Assess the morphology of the erythrocytes.
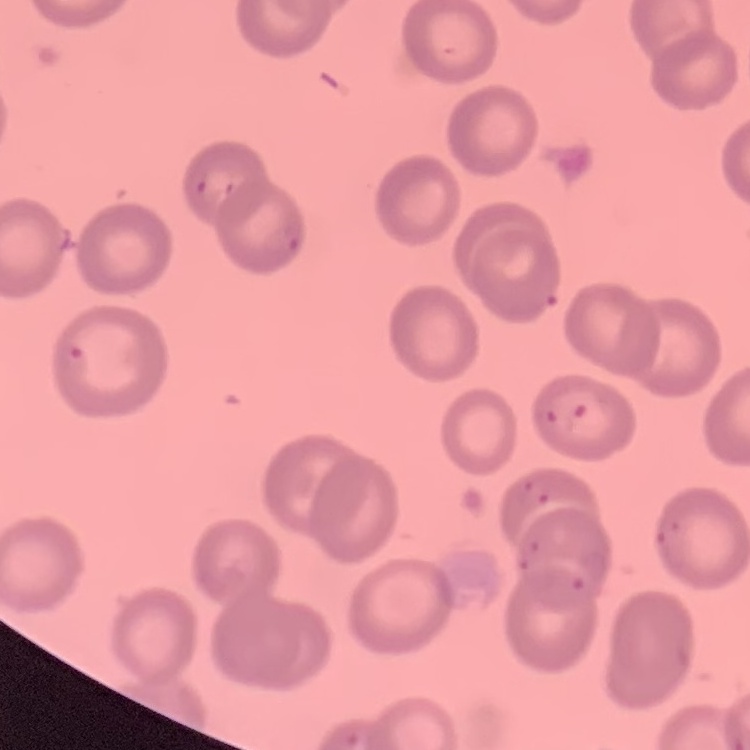

No rouleaux formation.

image type = square crop of a larger photomicrograph
preparation = thin blood film
stain = Field's or Giemsa